Report the malaria status of this cell.
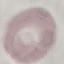

Uninfected.

Automatically extracted cell patch, resized to 64 × 64 pixels. Thin blood film. Acquired by smartphone through the microscope eyepiece. Giemsa-stained preparation.